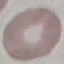

result = no malaria parasites detected
preparation = thin blood smear
stain = Giemsa
image type = cell patch, automatically extracted from a larger field of view and resized to 64 × 64 pixels
capture = smartphone camera at the microscope eyepiece